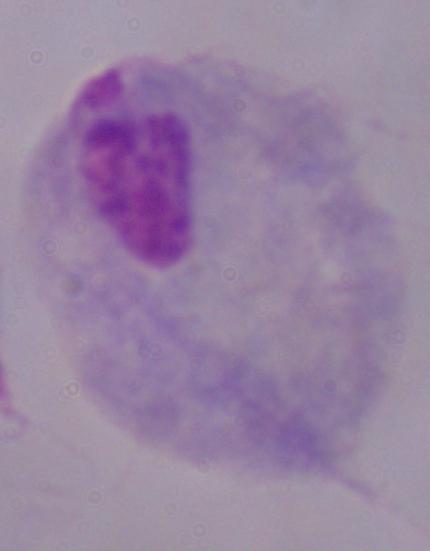
Micrograph. A trichomonad is seen. Captured at 1000x magnification.